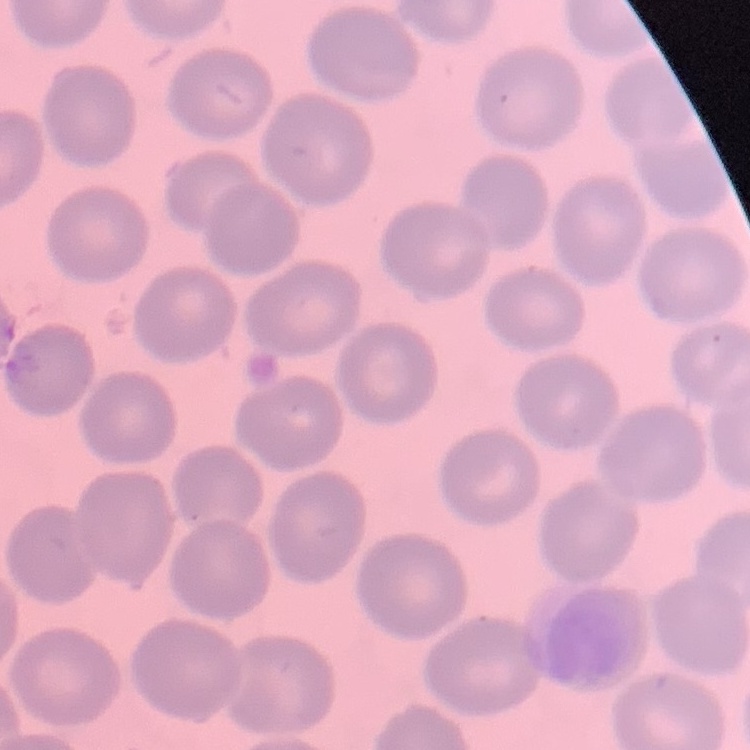
The erythrocytes exhibit no rouleaux formation. Stained with either Field's or Giemsa. Thin blood smear. Square crop of a larger photomicrograph.